Assess this cell for malaria.
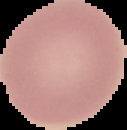
It is uninfected.

image type = segmented cell region on a black background
preparation = thin blood smear
image size = 127×130 pixels